Assess this cell for malaria.
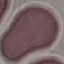

It is uninfected.

Summary:
  - Capture: smartphone camera at the microscope eyepiece
  - Image type: automatically extracted cell patch, resized to 64 × 64 pixels
  - Preparation: thin blood film
  - Stain: Giemsa